Identify the parasite.
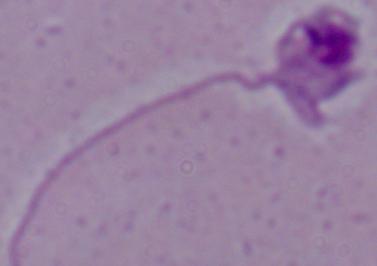

Leishmania.

Summary:
  - Modality: micrograph
  - Magnification: 1000x